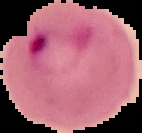
Summary:
  - Malaria status: parasitized
  - Preparation: thin blood film
  - Image size: 142×133 pixels
  - Image type: segmented cell region on a black background